Assess the morphology of the erythrocytes.
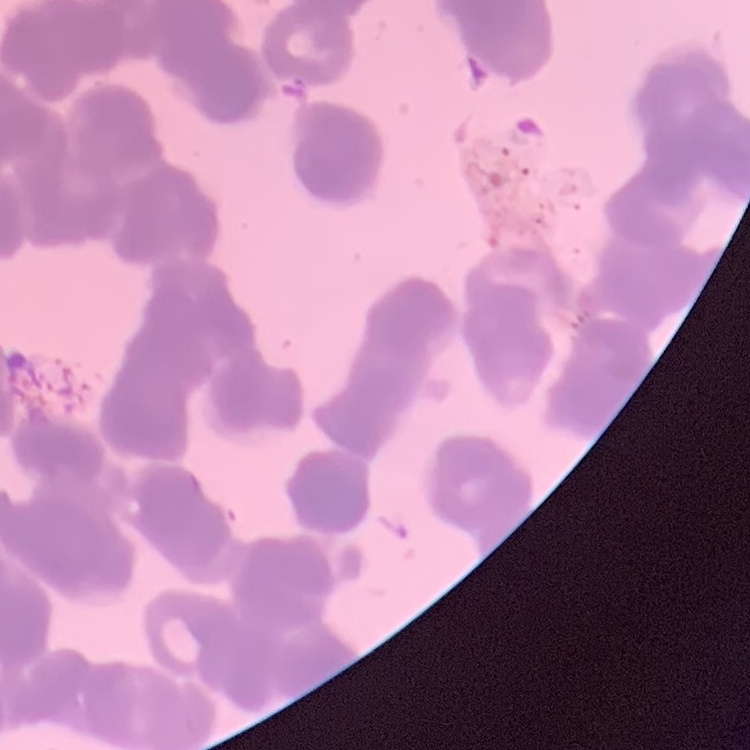

Rouleaux formation.

Thin blood smear. Field's or Giemsa stain. Square crop of a larger photomicrograph.